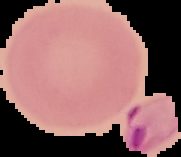

Summary:
  - Result: no malaria parasites seen
  - Image size: 181×157 pixels
  - Preparation: thin blood film
  - Image type: segmented cell region on a black background